Name the parasite shown.
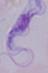

This is a trypanosome.

Photomicrograph. Captured at 1000x magnification.